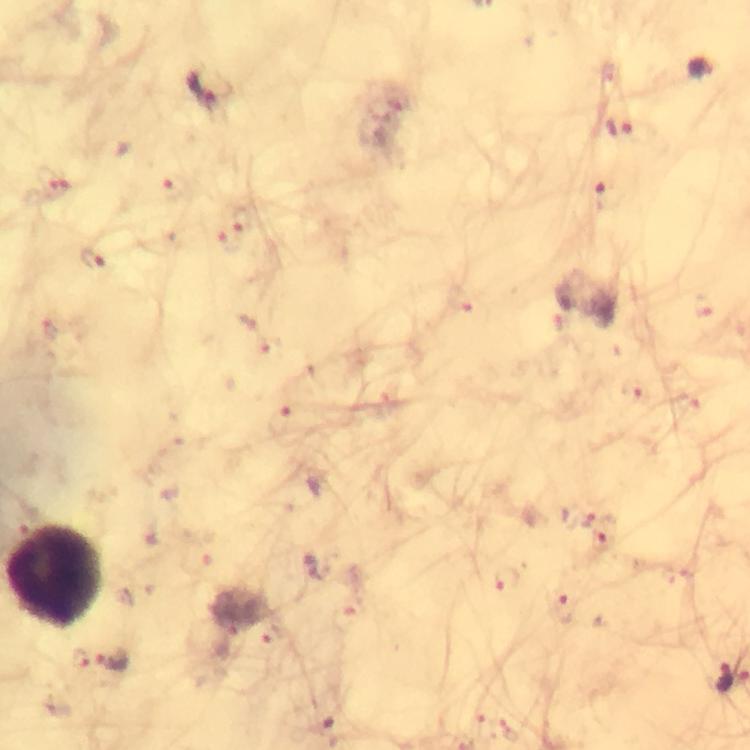
Approximate centers as (x, y) in pixels.
Summary:
  - Leukocyte locations: (58, 574)
  - Malaria parasite locations: (700, 69), (209, 86), (622, 130), (52, 181), (175, 189), (606, 197), (244, 220), (229, 241), (91, 259), (460, 303), (705, 307), (635, 391), (281, 421), (577, 518), (602, 540), (314, 566), (507, 578), (564, 609), (271, 636), (81, 658), (114, 662), (725, 676)
  - Cropped from: one field of view
  - Image size: 750×750 pixels
  - Magnification: 100x
  - Preparation: thick blood film
  - Immersion oil: used
  - Capture: smartphone mounted on the microscope
  - Stain: Giemsa
  - Context: from a diagnostic examination for malaria